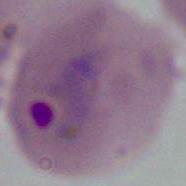
Summary:
  - Magnification: 400x or 1000x
  - Identification: Plasmodium
  - Modality: micrograph